Identify the preparation type.
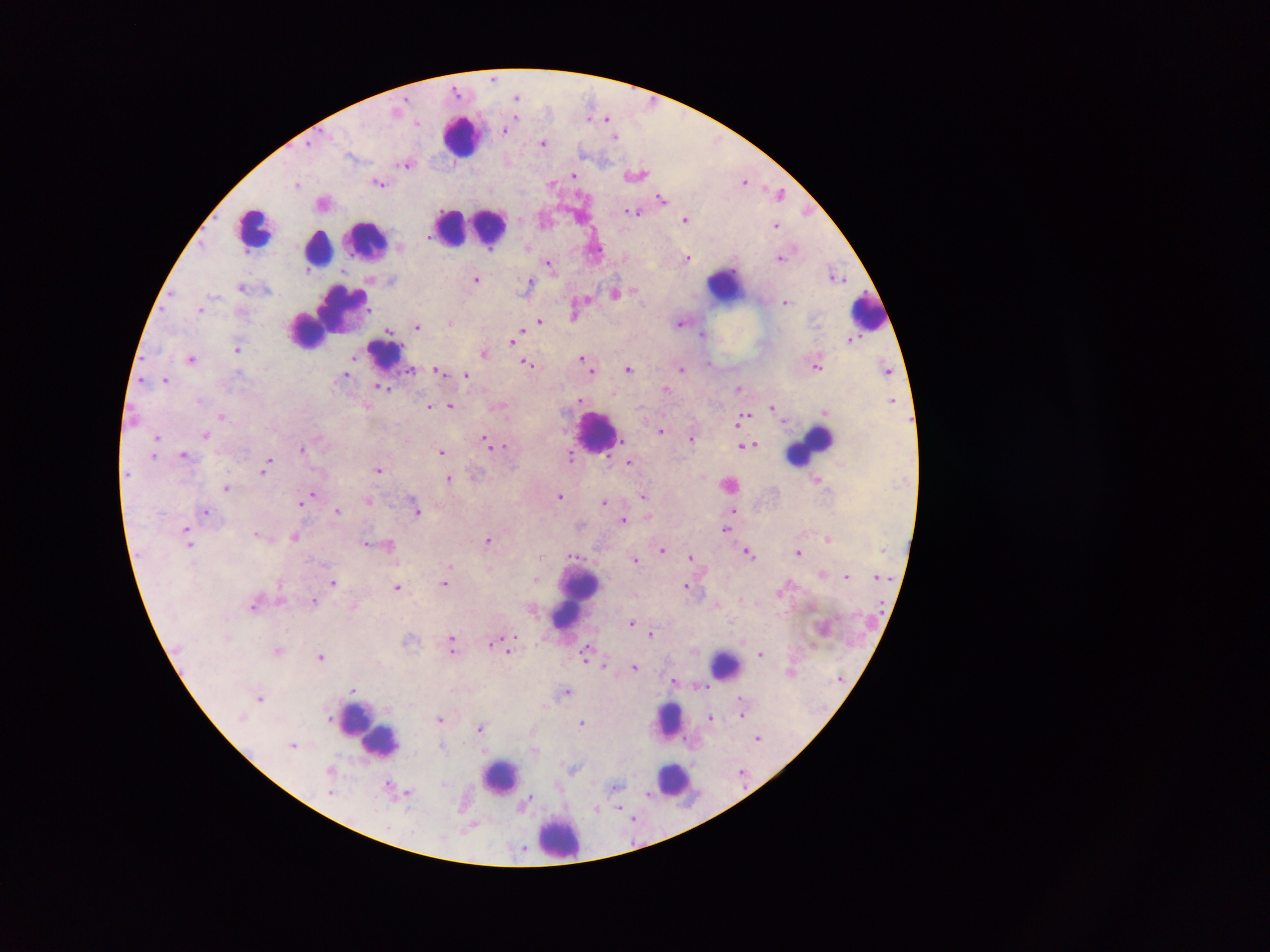

Thick blood smear.

Approximate centers as [x, y] in pixels.
Summary:
  - Plasmodium parasite locations: [494, 80], [457, 93], [517, 99], [604, 120], [419, 124], [610, 125], [506, 131], [615, 136], [544, 145], [407, 167], [574, 176], [745, 183], [551, 184], [380, 185], [297, 186], [780, 194], [662, 199], [635, 214], [685, 221], [777, 226], [687, 259], [780, 259], [549, 267], [477, 281], [531, 285], [243, 289], [616, 294], [787, 304], [201, 312], [575, 318], [540, 323], [450, 324], [681, 325], [418, 328], [390, 332], [703, 336], [517, 338], [513, 342], [238, 351], [485, 355], [354, 359], [582, 359], [191, 362], [529, 364], [586, 368], [818, 368], [591, 371], [628, 371], [682, 371], [441, 372], [460, 375], [347, 377], [466, 377], [166, 382], [384, 388], [666, 390], [738, 390], [580, 401], [199, 403], [451, 407], [429, 408], [772, 409], [223, 417], [742, 419], [661, 433], [207, 436], [158, 439], [692, 441], [486, 443], [748, 446], [302, 450], [442, 453], [184, 456], [571, 458], [630, 463], [268, 465], [264, 470], [380, 472], [450, 480], [817, 482], [729, 487], [226, 489], [311, 497], [644, 497], [561, 498], [303, 502], [369, 502], [604, 504], [417, 512], [338, 513], [206, 514], [624, 521], [581, 527], [727, 529], [187, 530], [256, 536], [295, 538], [828, 540], [488, 542], [366, 545], [190, 546], [389, 547], [664, 552], [750, 554], [799, 554], [574, 556], [541, 558], [691, 558], [636, 562], [449, 567], [823, 575], [847, 578], [879, 578], [537, 581], [333, 584], [446, 585], [686, 587], [398, 589], [782, 593], [280, 597], [315, 603], [256, 606], [532, 611], [632, 624], [825, 631], [652, 635], [409, 643], [493, 644], [453, 645], [180, 650], [509, 651], [279, 652], [696, 653], [760, 655], [585, 658], [321, 659], [604, 666], [635, 669], [793, 674], [839, 680], [674, 683], [703, 686], [353, 691], [566, 693], [261, 700], [741, 702], [742, 706], [389, 710], [743, 714], [243, 719], [329, 719], [712, 719], [440, 721], [583, 724], [481, 729], [533, 732], [759, 740], [294, 747], [443, 749], [483, 751], [534, 752], [574, 771], [332, 772], [743, 775], [445, 784], [558, 787], [616, 789], [332, 793], [406, 795], [649, 796], [526, 804], [465, 805], [596, 810], [633, 820], [471, 829], [523, 852]
  - Leukocyte locations (subset; some below the resolvable size): [461, 140], [470, 228], [253, 230], [365, 242], [316, 252], [727, 287], [868, 315], [326, 319], [385, 355], [597, 435], [810, 447], [575, 600], [724, 666], [355, 720], [668, 722], [378, 743], [501, 778], [672, 782], [558, 839]
  - Country: Ghana
  - Field of view: single
  - Image size: 1270×952 pixels
  - Capture: mobile-phone photograph through a microscope